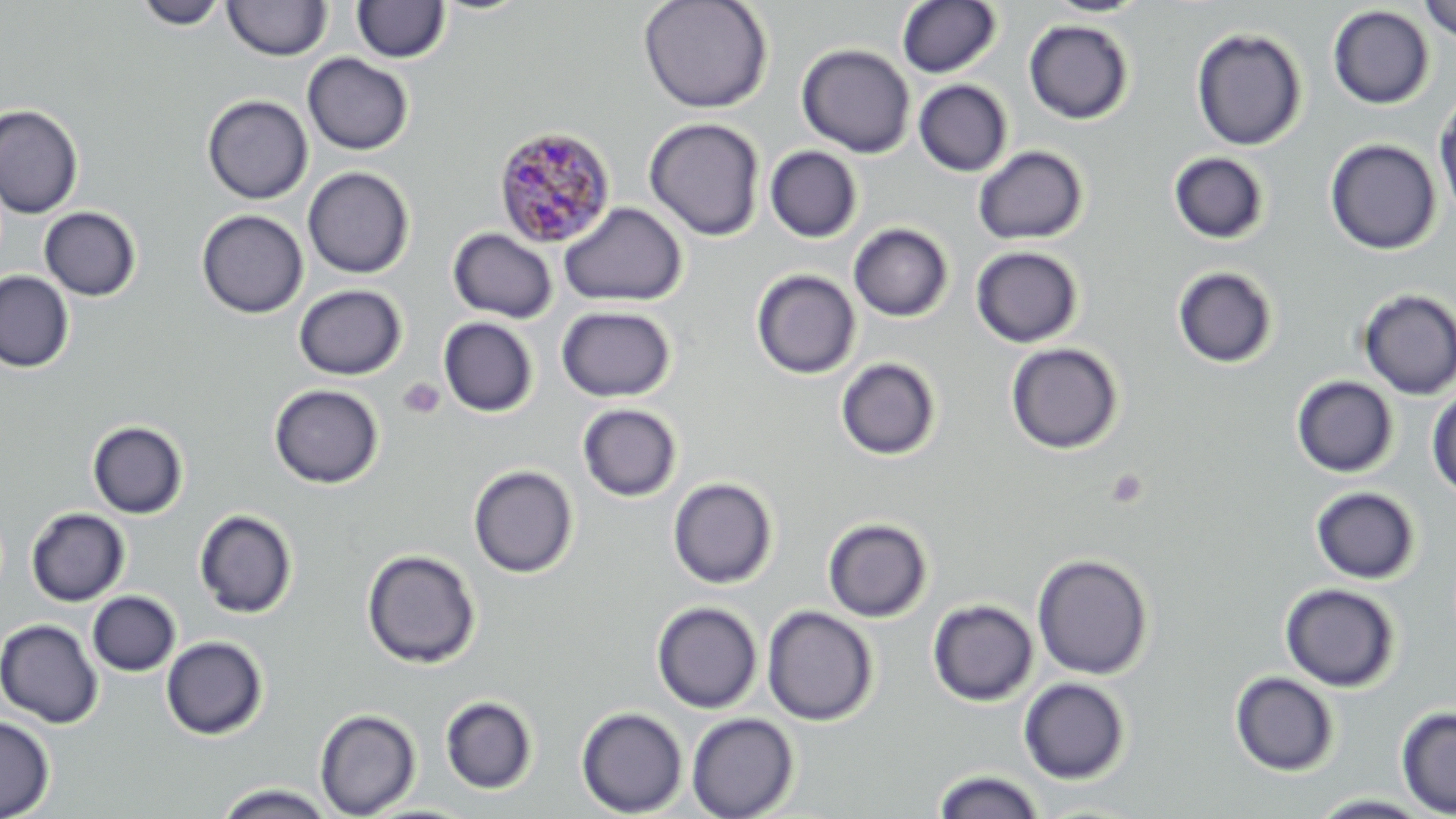

slide-level diagnosis = Plasmodium malariae
field of view = one of a larger specimen
preparation = thin blood film
uninfected red blood cell locations = approximate bounding boxes as named x1/y1/x2/y2 corners in pixels: (x1=134, y1=0, x2=229, y2=30), (x1=638, y1=0, x2=774, y2=114), (x1=1042, y1=0, x2=1151, y2=18), (x1=1418, y1=0, x2=1456, y2=42), (x1=223, y1=1, x2=332, y2=61), (x1=351, y1=1, x2=451, y2=63), (x1=896, y1=1, x2=1002, y2=78), (x1=1328, y1=5, x2=1434, y2=110), (x1=1024, y1=19, x2=1134, y2=124), (x1=1190, y1=27, x2=1307, y2=151), (x1=796, y1=43, x2=915, y2=158), (x1=302, y1=53, x2=414, y2=155), (x1=913, y1=79, x2=1013, y2=176), (x1=1434, y1=91, x2=1456, y2=224), (x1=202, y1=95, x2=314, y2=204), (x1=0, y1=104, x2=83, y2=219), (x1=644, y1=117, x2=765, y2=241), (x1=1324, y1=138, x2=1442, y2=254), (x1=973, y1=145, x2=1088, y2=245), (x1=765, y1=146, x2=862, y2=242), (x1=1168, y1=152, x2=1270, y2=244), (x1=302, y1=167, x2=415, y2=279), (x1=558, y1=202, x2=688, y2=307), (x1=39, y1=206, x2=141, y2=301), (x1=197, y1=209, x2=308, y2=318), (x1=849, y1=223, x2=954, y2=322), (x1=448, y1=228, x2=558, y2=323), (x1=971, y1=246, x2=1083, y2=348), (x1=1172, y1=266, x2=1279, y2=369), (x1=751, y1=269, x2=861, y2=379), (x1=0, y1=270, x2=74, y2=372), (x1=293, y1=284, x2=407, y2=380), (x1=1357, y1=288, x2=1456, y2=400), (x1=556, y1=305, x2=676, y2=402), (x1=438, y1=317, x2=538, y2=417), (x1=1005, y1=343, x2=1124, y2=454), (x1=836, y1=357, x2=941, y2=460), (x1=1291, y1=375, x2=1399, y2=477), (x1=268, y1=383, x2=384, y2=489), (x1=1427, y1=387, x2=1456, y2=500), (x1=577, y1=403, x2=682, y2=502), (x1=87, y1=420, x2=189, y2=519), (x1=468, y1=465, x2=578, y2=578), (x1=667, y1=477, x2=778, y2=589), (x1=1310, y1=486, x2=1420, y2=585), (x1=26, y1=508, x2=130, y2=606), (x1=193, y1=508, x2=298, y2=619), (x1=823, y1=518, x2=933, y2=622), (x1=361, y1=548, x2=481, y2=669), (x1=1032, y1=553, x2=1154, y2=679), (x1=1280, y1=583, x2=1401, y2=692), (x1=87, y1=591, x2=180, y2=676), (x1=928, y1=599, x2=1038, y2=706), (x1=651, y1=601, x2=763, y2=713), (x1=762, y1=605, x2=879, y2=726), (x1=0, y1=619, x2=103, y2=729), (x1=161, y1=635, x2=268, y2=740), (x1=1229, y1=671, x2=1340, y2=776), (x1=1018, y1=677, x2=1131, y2=784), (x1=440, y1=695, x2=537, y2=794), (x1=576, y1=707, x2=688, y2=817), (x1=1395, y1=707, x2=1456, y2=817), (x1=314, y1=708, x2=421, y2=817), (x1=686, y1=713, x2=799, y2=819), (x1=0, y1=715, x2=55, y2=818), (x1=932, y1=769, x2=1045, y2=819), (x1=213, y1=783, x2=338, y2=819), (x1=1307, y1=794, x2=1437, y2=818)
modality = light microscopy
magnification = 1000x
stain = May-Grünwald-Giemsa
Plasmodium malariae-infected red blood cell locations = approximate bounding boxes as named x1/y1/x2/y2 corners in pixels: (x1=492, y1=125, x2=617, y2=247)
image size = 1456×819 pixels
platelet locations = approximate bounding boxes as named x1/y1/x2/y2 corners in pixels: (x1=397, y1=377, x2=445, y2=420), (x1=1105, y1=468, x2=1148, y2=509)